Report the malaria status of this cell.
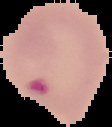
Parasitized.

Image is 112×127 pixels. Segmented cell region on a black background. From a thin blood film.